State which parasite is depicted.
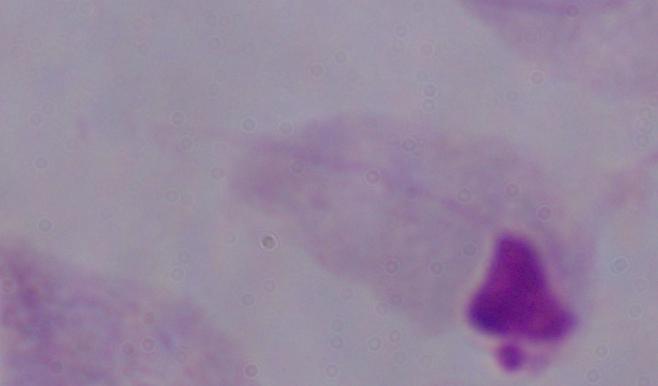
A trichomonad.

1000x magnification. Photomicrograph.